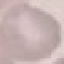

Summary:
  - Malaria status: uninfected
  - Image type: automatically extracted cell patch, resized to 64 × 64 pixels
  - Capture: smartphone camera at the microscope eyepiece
  - Preparation: thin blood film
  - Stain: Giemsa